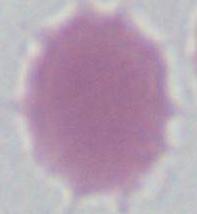
magnification = 1000x
modality = micrograph
identification = red blood cell